Assess this cell for malaria.
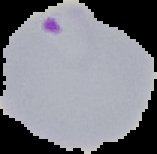

It is parasitized.

image size = 157×154 pixels
image type = cell region segmented out of the field of view; surrounding area masked to black
preparation = thin blood smear